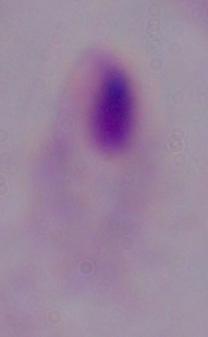

Summary:
  - Identification: trichomonad
  - Modality: photomicrograph
  - Magnification: 1000x